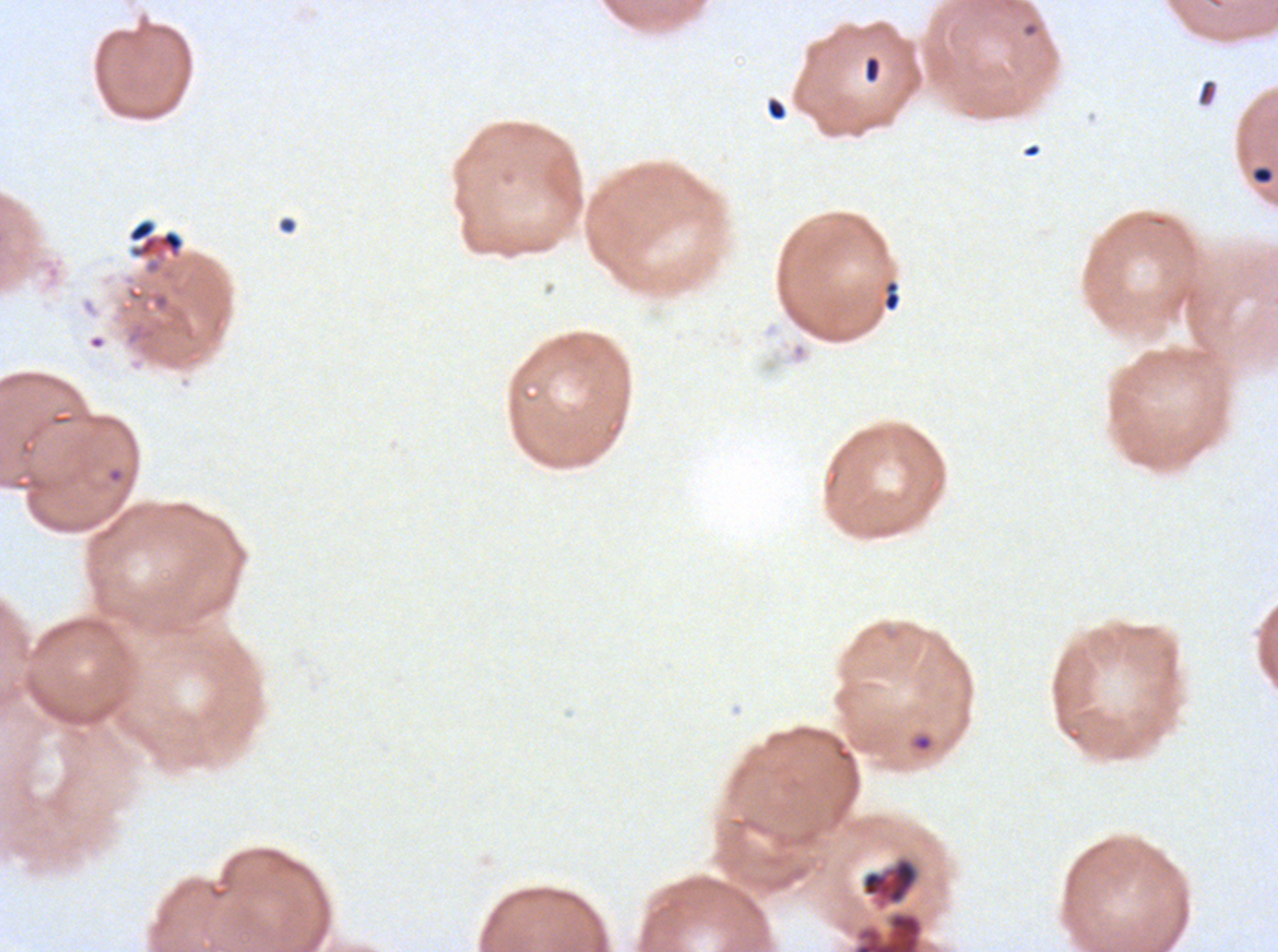

notation = approximate bounding boxes as [x1, y1, x2, y2] in pixels
debris locations = [864, 55, 881, 83], [1197, 79, 1218, 106], [766, 98, 787, 121], [277, 215, 297, 235], [127, 218, 185, 259], [882, 280, 902, 312], [861, 856, 920, 911]
ring locations = [1251, 165, 1274, 185], [105, 466, 125, 484], [910, 733, 934, 752]
specimen = P. falciparum cultured ex vivo for 24 to 48 hours, from a patient in The Gambia
field of view = sub-image separated from a larger composite
image size = 1278×952 pixels
stain = Giemsa
preparation = thin blood film